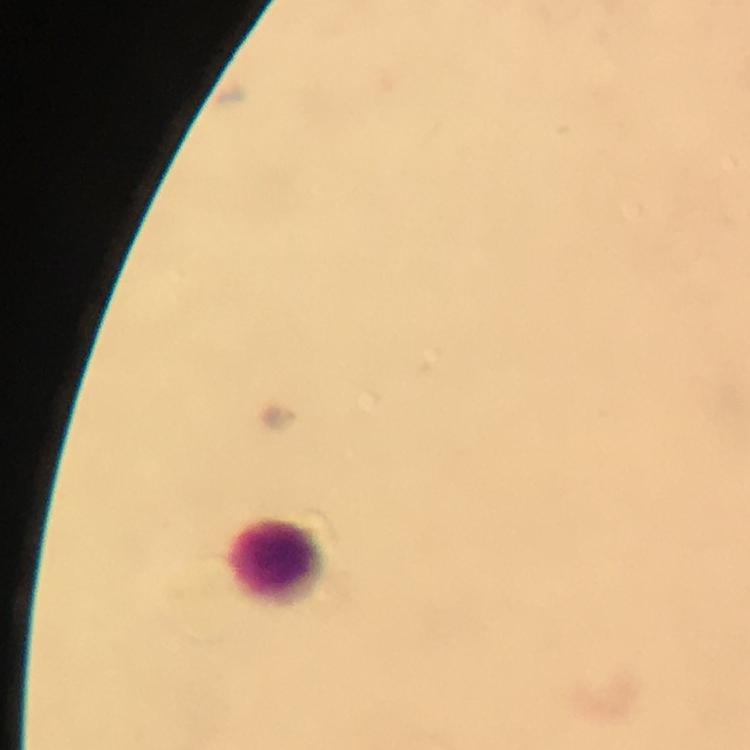
Approximate centers as (x, y) in pixels.
Summary:
  - Leukocyte locations: (274, 564)
  - Capture: smartphone mounted on the microscope
  - Cropped from: one field of view
  - Context: from a malaria diagnostic workup
  - Preparation: thick blood smear
  - Immersion oil: applied
  - Magnification: 100x
  - Image size: 750×750 pixels
  - Malaria parasites: none detected
  - Stain: Giemsa